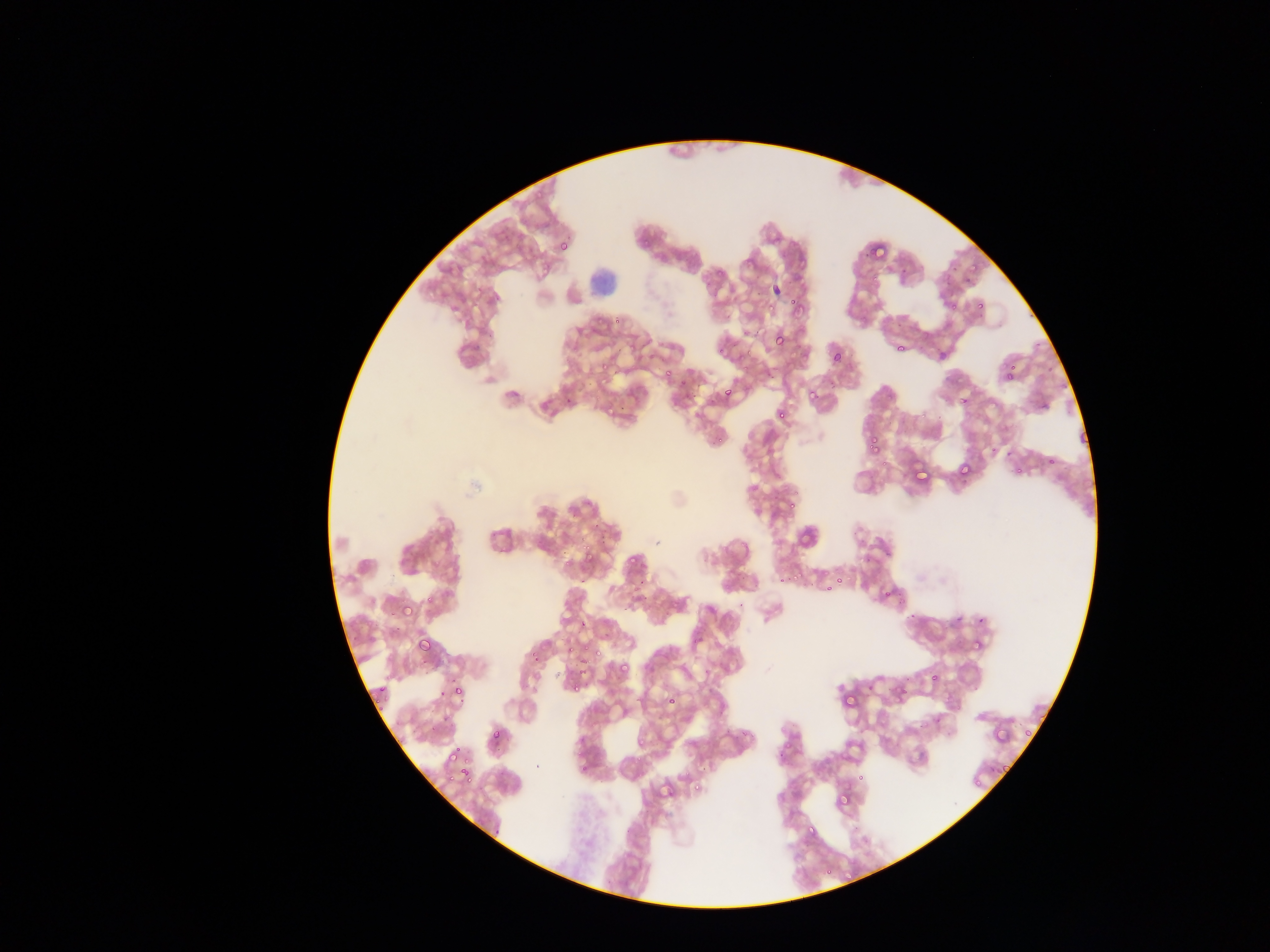

Approximate bounding boxes as left top right bottom in pixels. Plasmodium parasite locations: 558 240 570 252; 870 244 891 260; 969 263 979 276; 899 267 913 276; 938 268 956 285; 771 284 782 295; 942 289 970 311; 785 294 799 309; 761 297 787 319; 976 300 984 309; 1027 311 1040 322; 609 317 624 326; 773 333 788 348; 1035 336 1048 351; 715 342 732 361; 895 344 905 353; 831 352 842 364; 1041 355 1059 370; 662 363 680 382; 599 368 615 387; 1003 371 1013 382; 721 389 731 400; 805 390 822 402; 564 392 579 408; 960 396 969 406; 603 400 620 415; 1036 402 1049 413; 777 406 790 423; 917 407 930 422; 709 430 730 449; 863 434 883 458; 990 439 996 454; 1003 449 1012 456; 1046 456 1057 469; 957 461 972 476; 913 462 930 483; 1009 462 1023 481; 787 500 796 511; 580 539 597 565; 623 548 640 568; 560 554 572 566; 788 566 801 583; 776 572 785 587; 832 572 843 583; 578 574 584 587; 627 578 645 593; 820 584 831 598; 879 587 896 601; 423 594 436 607; 402 605 414 618; 953 607 968 626; 906 610 918 623; 977 610 990 627; 576 615 591 629; 693 634 702 643; 418 636 433 651; 564 637 582 661; 969 640 982 653; 592 645 603 660; 616 648 636 671; 530 651 540 661; 888 671 916 702; 930 674 938 683; 436 681 449 698; 571 681 584 691; 374 685 387 696; 452 686 463 698; 846 693 857 705; 665 694 677 705; 372 697 388 712; 489 722 506 744; 1020 722 1039 739; 427 723 434 734; 578 735 587 745; 633 736 647 747; 443 739 458 759; 456 757 469 782; 994 761 1013 773; 444 769 454 780; 854 771 868 783; 968 771 984 786; 691 783 707 795; 837 789 854 805; 776 793 786 803; 805 820 815 837; 490 828 506 839. Leukocyte locations: 582 266 623 304. Sample from Ghana. Image is 1270×952 pixels. Mobile-phone photograph taken through the microscope. Single field of view. Thin blood smear.